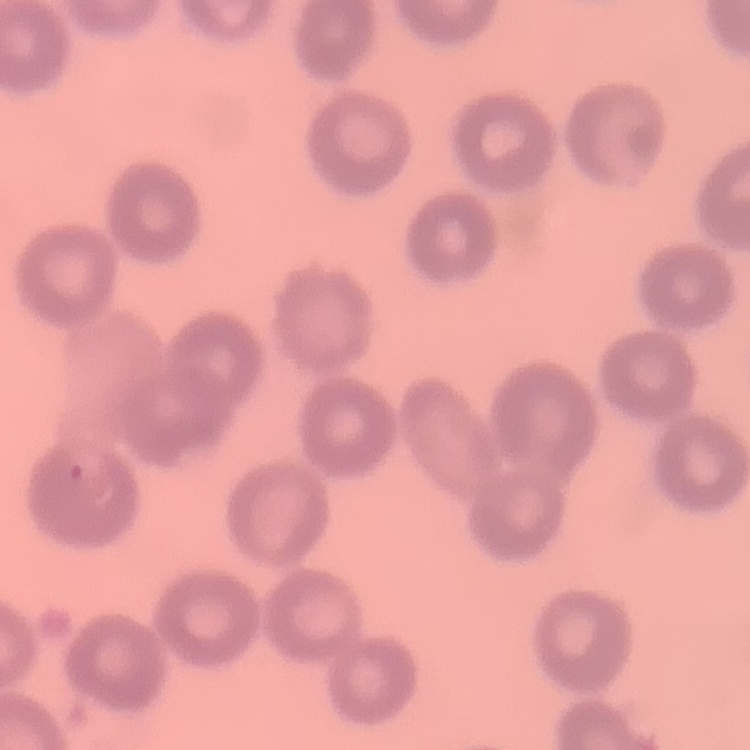
red blood cell morphology = no rouleaux formation
stain = Field's or Giemsa
preparation = thin peripheral smear
image type = one tile cut from a larger photomicrograph